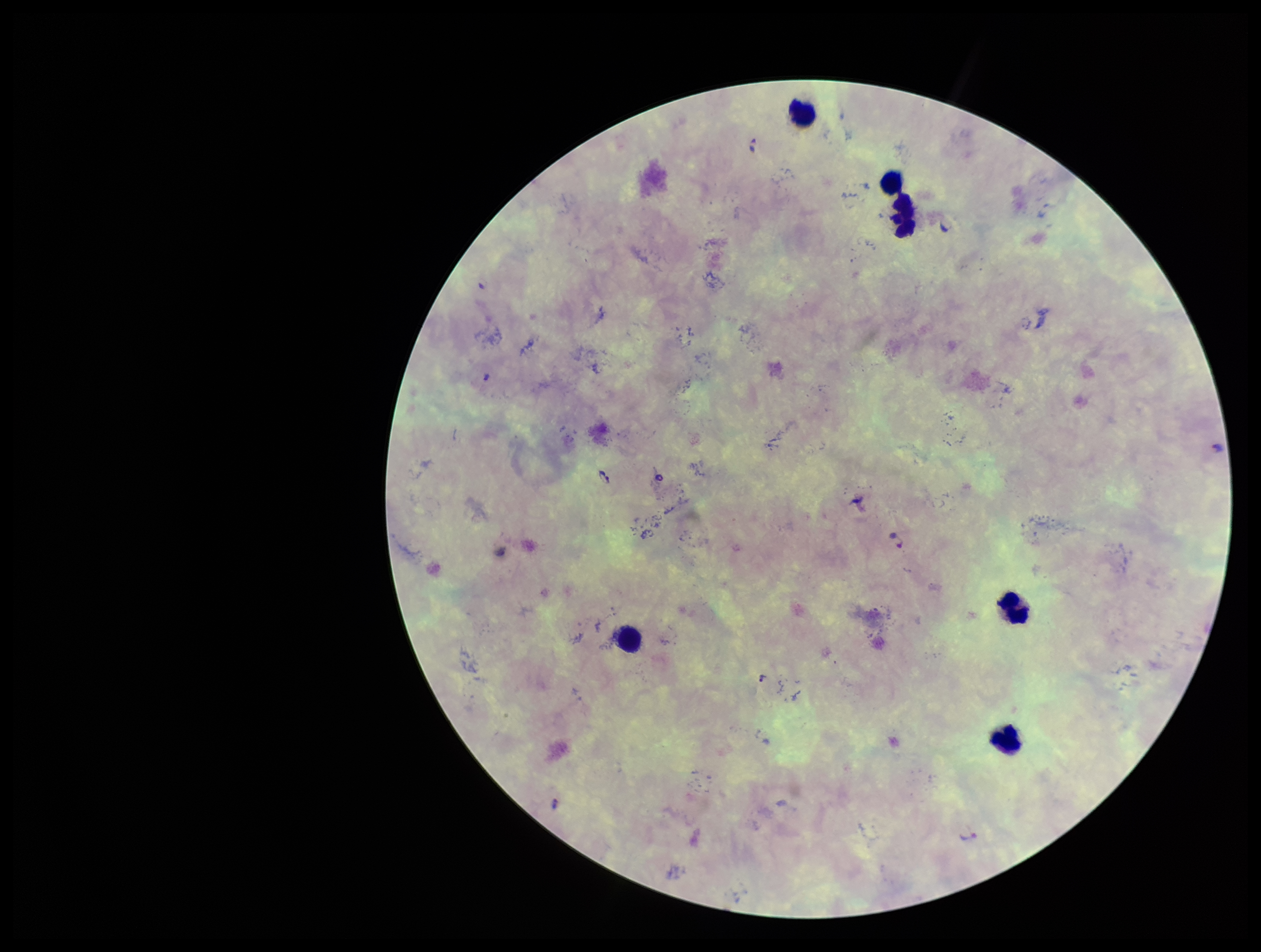
leukocyte count = 6
field of view = one from this slide
stain = Giemsa
capture = smartphone photograph through the microscope eyepiece
species reported for this patient = Plasmodium falciparum
Plasmodium parasites = detected
patient malaria status = infected
preparation = thick
image size = 1261×952 pixels
parasite count = 2